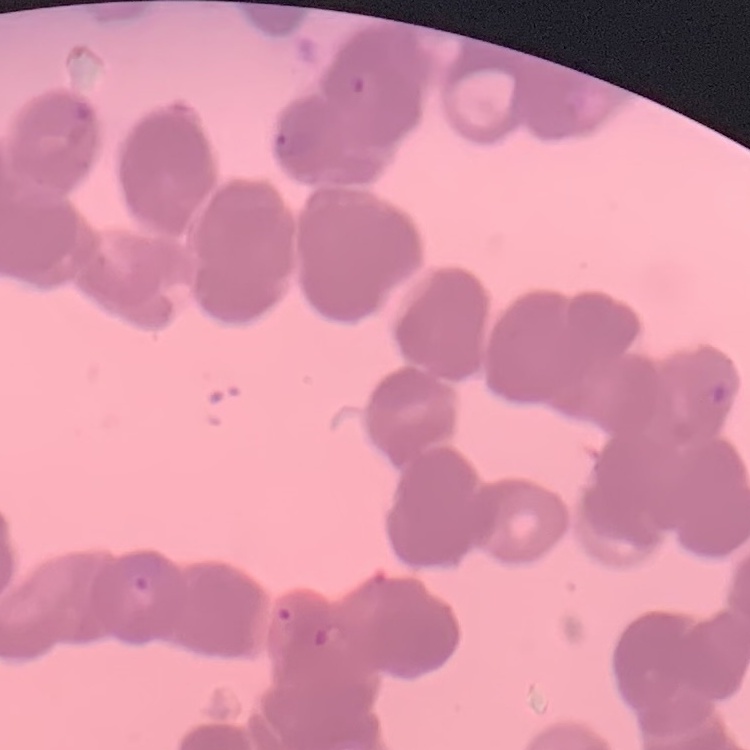

The red blood cells show rouleaux formation. Field's or Giemsa stain. Thin peripheral smear. Square crop of a larger photomicrograph.